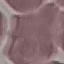
Malaria status: uninfected. Thin blood smear. Photographed with a smartphone camera at the microscope eyepiece. Cell patch, automatically extracted from a larger field of view and resized to 64 × 64 pixels. Giemsa-stained preparation.